Name the cell type shown.
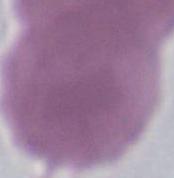
This is an erythrocyte.

Summary:
  - Magnification: 1000x
  - Modality: photomicrograph